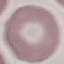

Result: no malaria parasites seen. Photographed with a smartphone camera at the microscope eyepiece. Cell patch, automatically extracted from a larger field of view and resized to 64 × 64 pixels. Thin blood film. Giemsa stain.